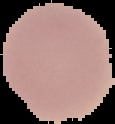

The area outside the segmented cell region is set to black. From a thin blood smear. Malaria status: uninfected. Image is 115×124 pixels.